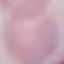
result: negative for malaria parasites
capture: smartphone through the microscope eyepiece
stain: Giemsa
image_type: cell patch, automatically extracted from a larger field of view and resized to 64 × 64 pixels
preparation: thin blood film